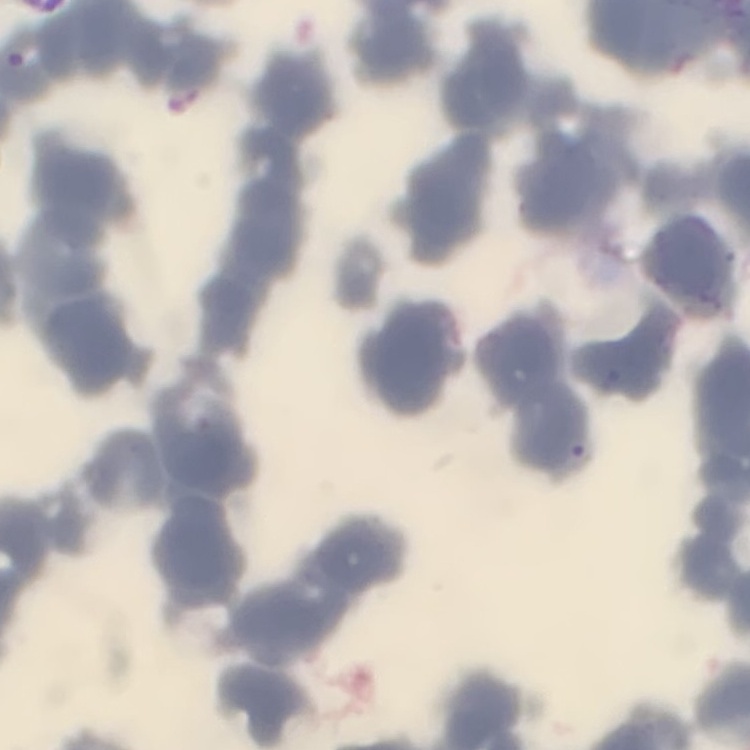

red_blood_cell_morphology: rouleaux formation
preparation: thin peripheral smear
image_type: square crop of a larger photomicrograph
stain: Field's or Giemsa